Classify this cell by malaria status.
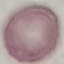
Uninfected.

Thin blood film. Giemsa stain. Acquired by smartphone through the microscope eyepiece. Automatically extracted cell patch, resized to 64 × 64 pixels.